Locate every blood parasite and identify its species.
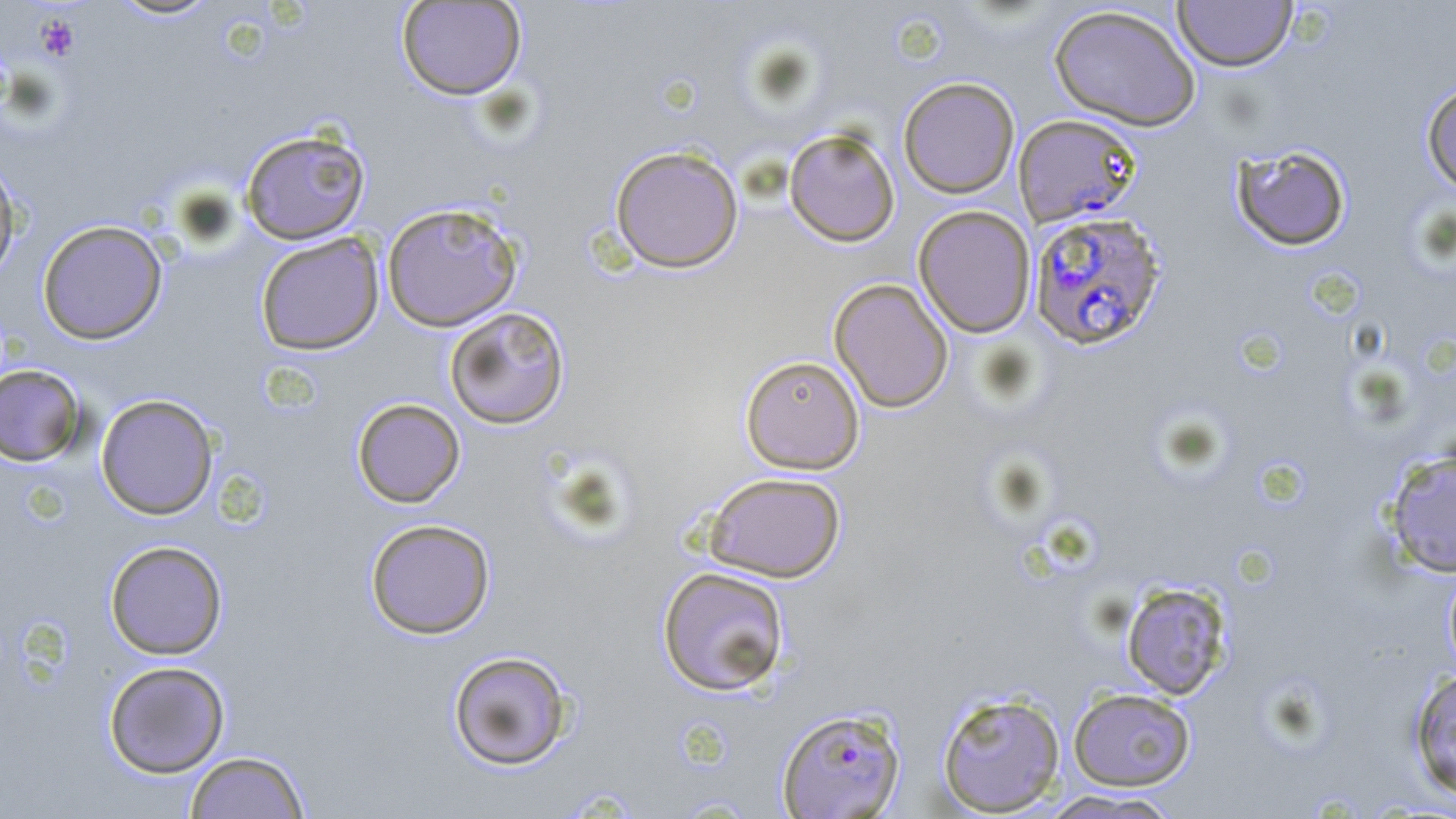
Approximate bounding boxes as (x1,y1)-(x2,y2) corner pairs in pixels.
Plasmodium falciparum-infected red blood cells: (1013,113)-(1143,228), (1028,211)-(1167,350), (777,707)-(905,818).
No Plasmodium ovale, Plasmodium malariae, Plasmodium vivax, Babesia divergens, or Trypanosoma brucei observed.

Uninfected red blood cell locations: (108,0)-(223,21), (1173,0)-(1298,72), (396,1)-(527,100), (1048,4)-(1202,131), (898,77)-(1020,198), (1421,81)-(1456,197), (783,127)-(901,247), (240,128)-(371,244), (1231,144)-(1352,251), (610,145)-(744,273), (0,155)-(22,285), (381,202)-(523,331), (912,205)-(1036,338), (37,220)-(167,344), (255,232)-(384,355), (829,277)-(954,412), (444,305)-(570,429), (740,354)-(865,474), (0,363)-(87,466), (95,394)-(219,520), (352,397)-(465,508), (1384,448)-(1456,578), (702,471)-(846,583), (365,517)-(496,639), (104,540)-(228,660), (1442,565)-(1456,681), (657,566)-(791,697), (1120,581)-(1234,700), (448,650)-(573,771), (103,660)-(230,778), (1407,667)-(1456,801), (1068,687)-(1196,791), (936,690)-(1066,816), (184,750)-(311,819), (1036,790)-(1185,818). Platelet locations: (35,13)-(80,61). Slide-level diagnosis: Plasmodium falciparum. 1000x magnification. Light microscopy. One field of a larger specimen. Image is 1456×819 pixels. Thin blood film. May-Grünwald-Giemsa-stained preparation.